Locate every uninfected red blood cell.
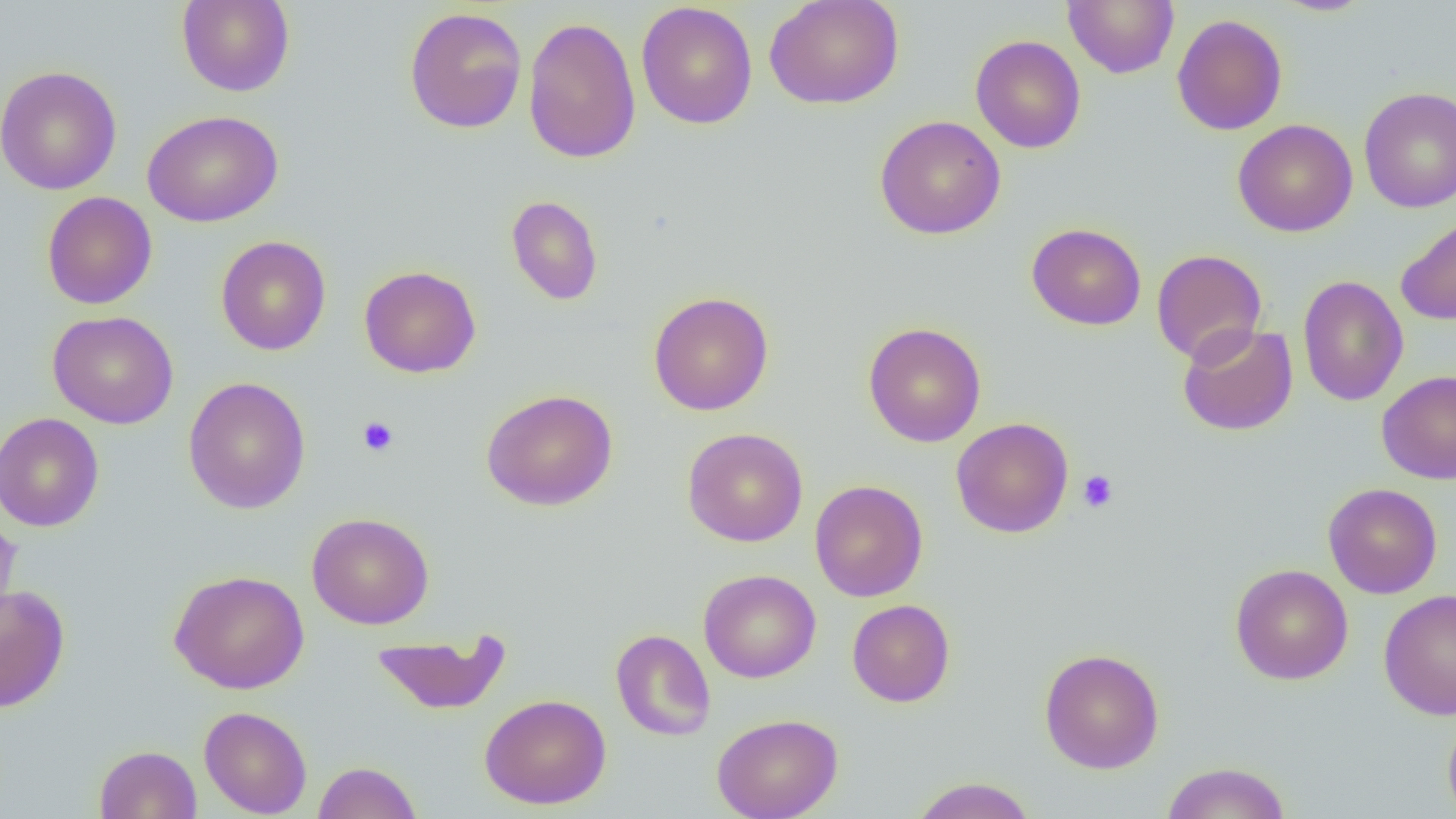

Approximate bounding boxes as named x1/y1/x2/y2 corners in pixels.
Uninfected red blood cells: (x1=764, y1=0, x2=904, y2=110), (x1=1063, y1=0, x2=1179, y2=79), (x1=1271, y1=0, x2=1375, y2=16), (x1=176, y1=1, x2=295, y2=97), (x1=636, y1=2, x2=758, y2=130), (x1=404, y1=6, x2=527, y2=134), (x1=1172, y1=14, x2=1287, y2=135), (x1=522, y1=16, x2=642, y2=164), (x1=970, y1=34, x2=1086, y2=153), (x1=1, y1=65, x2=122, y2=195), (x1=1359, y1=87, x2=1456, y2=212), (x1=142, y1=110, x2=283, y2=227), (x1=875, y1=115, x2=1006, y2=240), (x1=1232, y1=119, x2=1358, y2=237), (x1=42, y1=191, x2=157, y2=310), (x1=506, y1=195, x2=604, y2=305), (x1=1396, y1=215, x2=1456, y2=326), (x1=1026, y1=222, x2=1147, y2=331), (x1=215, y1=235, x2=331, y2=355), (x1=1151, y1=249, x2=1267, y2=365), (x1=359, y1=265, x2=481, y2=378), (x1=1297, y1=275, x2=1408, y2=407), (x1=648, y1=291, x2=775, y2=416), (x1=47, y1=310, x2=179, y2=429), (x1=862, y1=322, x2=986, y2=447), (x1=1177, y1=322, x2=1298, y2=436), (x1=1377, y1=370, x2=1456, y2=484), (x1=183, y1=376, x2=311, y2=514), (x1=481, y1=389, x2=618, y2=511), (x1=1, y1=412, x2=104, y2=532), (x1=951, y1=417, x2=1074, y2=538), (x1=682, y1=427, x2=808, y2=547), (x1=809, y1=480, x2=928, y2=602), (x1=1323, y1=482, x2=1442, y2=599), (x1=0, y1=511, x2=22, y2=634), (x1=307, y1=512, x2=435, y2=629), (x1=1230, y1=563, x2=1353, y2=685), (x1=169, y1=569, x2=309, y2=694), (x1=699, y1=569, x2=821, y2=683), (x1=0, y1=584, x2=70, y2=714), (x1=1378, y1=589, x2=1456, y2=721), (x1=846, y1=599, x2=956, y2=707), (x1=370, y1=629, x2=511, y2=715), (x1=610, y1=629, x2=716, y2=741), (x1=1039, y1=648, x2=1165, y2=773), (x1=480, y1=693, x2=611, y2=809), (x1=198, y1=705, x2=312, y2=818), (x1=1442, y1=712, x2=1456, y2=819), (x1=712, y1=713, x2=844, y2=819), (x1=93, y1=745, x2=202, y2=819), (x1=312, y1=760, x2=422, y2=819), (x1=1159, y1=761, x2=1293, y2=819), (x1=910, y1=777, x2=1037, y2=819).

Platelet locations: (x1=358, y1=416, x2=399, y2=457), (x1=1077, y1=470, x2=1119, y2=513). Slide-level diagnosis: negative for blood parasites. Light microscopy. Thin blood smear. 1000x magnification. Image is 1456×819 pixels. Single field of view.